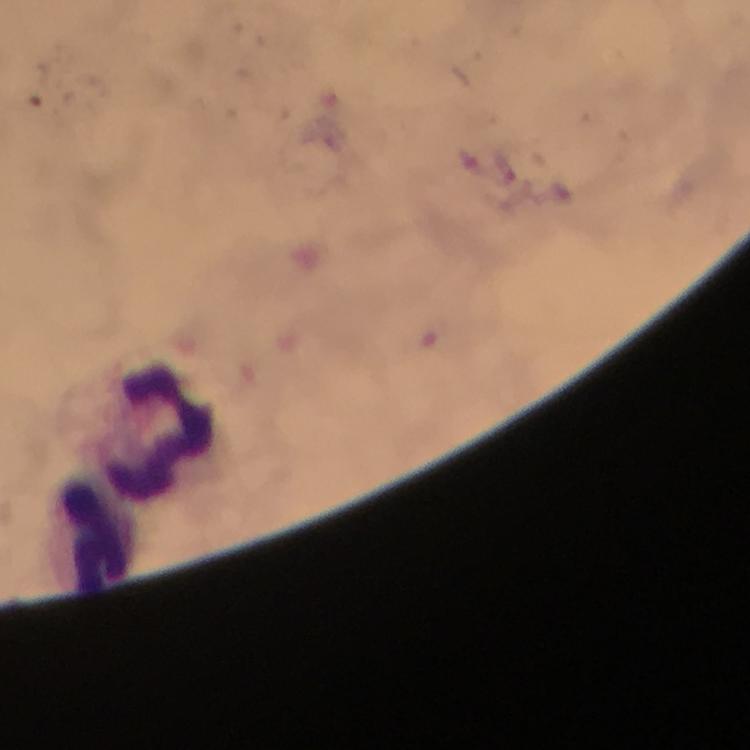

immersion oil = applied
preparation = thick smear
stain = Giemsa
leukocyte locations = approximate centers as [x, y] in pixels: [163, 432], [100, 540]
malaria parasites = none detected
cropped from = a single field of view
image size = 750×750 pixels
context = from a diagnostic examination for malaria
capture = smartphone camera through the microscope
magnification = 100x